Identify the cell.
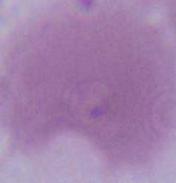
An erythrocyte.

1000x magnification. Photomicrograph.